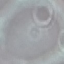

Summary:
  - Result: no malaria parasites seen
  - Stain: Giemsa
  - Preparation: thin blood film
  - Image type: automatically extracted cell patch, resized to 64 × 64 pixels
  - Capture: smartphone camera at the microscope eyepiece